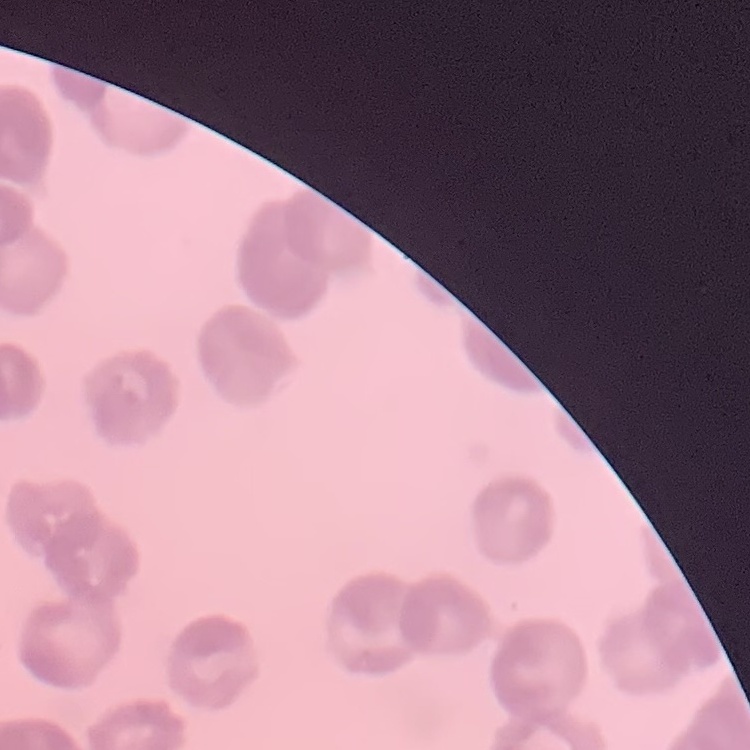

{
  "red_blood_cell_morphology": "rouleaux formation",
  "image_type": "one tile cut from a larger photomicrograph",
  "stain": "Field's or Giemsa",
  "preparation": "thin blood film"
}